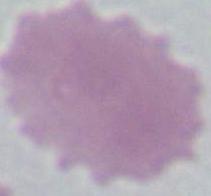

Photomicrograph. 1000x magnification. An erythrocyte is shown.